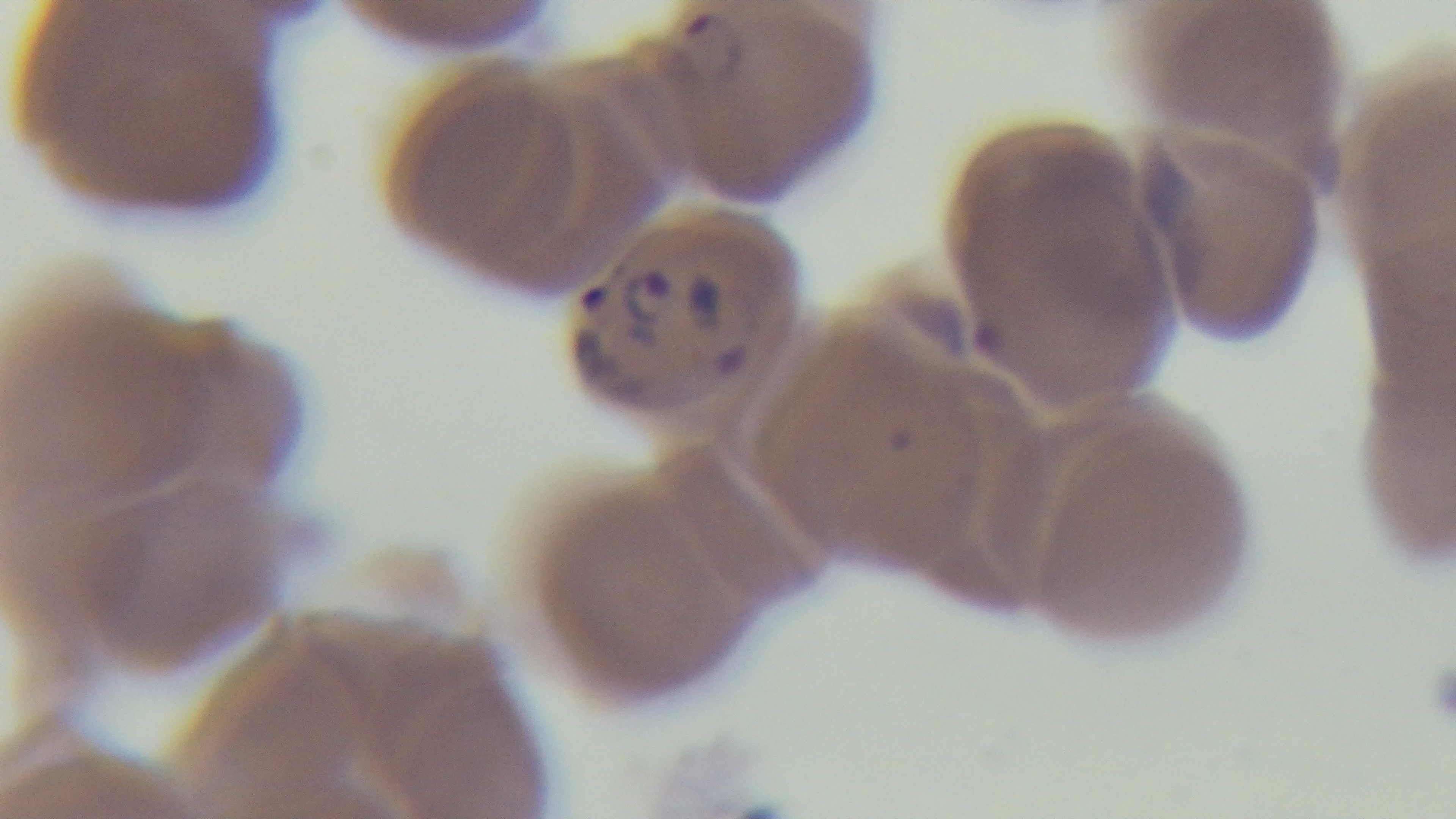

Summary:
  - Malaria status: infected
  - Modality: light microscopy
  - Preparation: thin blood film
  - Field of view: one from the slide
  - Stain: Giemsa
  - Capture: mounted 4K digital camera
  - Objective: 100x oil immersion